Locate every blood parasite and identify its species.
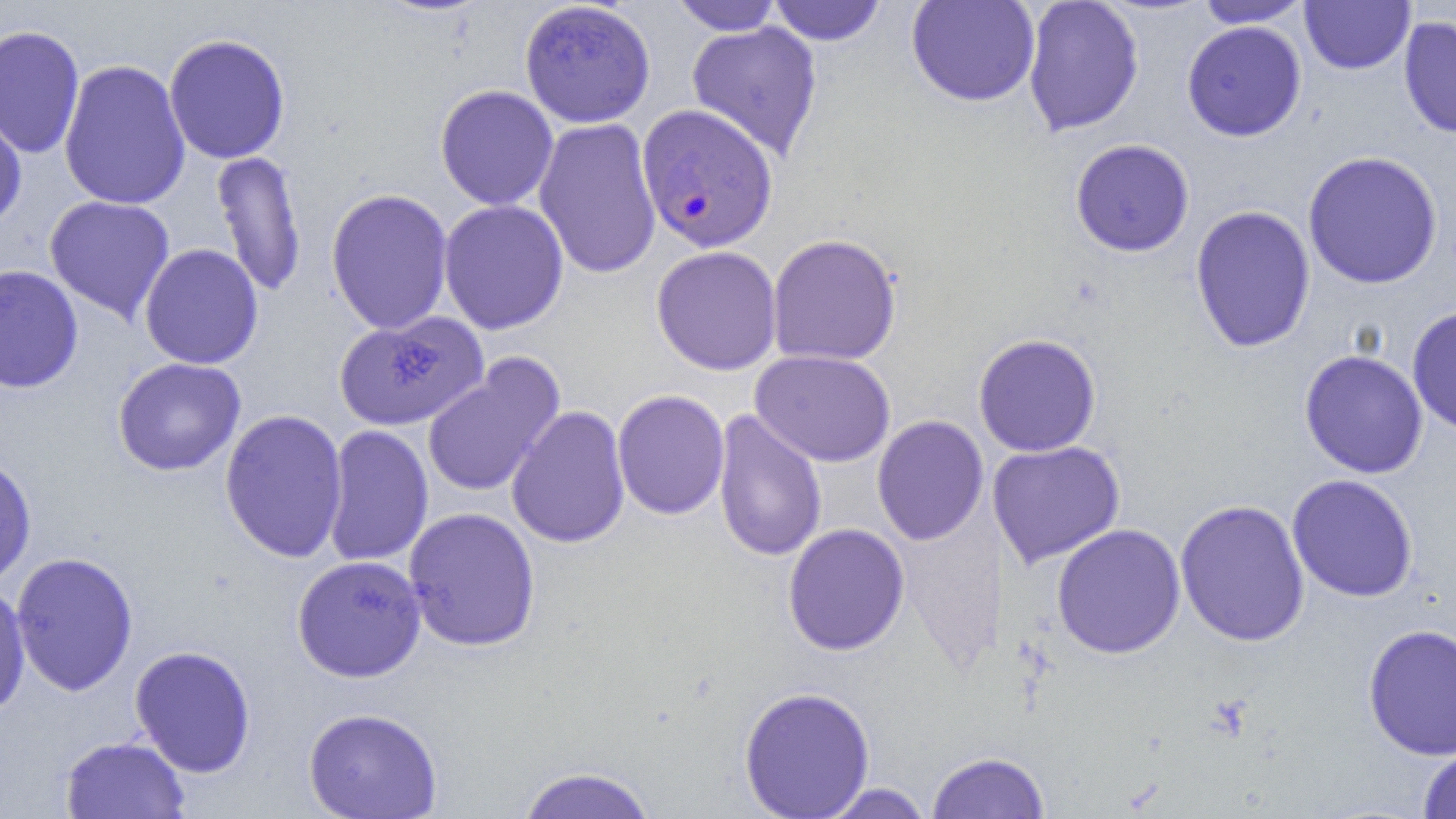

Approximate bounding boxes as (x1, y1, x2, y2) in pixels.
Plasmodium falciparum-infected red blood cells: (636, 104, 778, 253).
No Plasmodium ovale, Plasmodium malariae, Plasmodium vivax, Babesia divergens, or Trypanosoma brucei observed.

Summary:
  - Uninfected red blood cell locations: (669, 0, 786, 35), (906, 0, 1041, 108), (1022, 0, 1145, 137), (1300, 0, 1416, 75), (519, 1, 656, 128), (766, 1, 888, 46), (1195, 1, 1313, 28), (1398, 15, 1456, 139), (1181, 20, 1307, 142), (686, 21, 823, 160), (0, 25, 86, 159), (164, 33, 291, 164), (58, 59, 191, 210), (434, 84, 559, 211), (0, 109, 27, 233), (533, 117, 662, 280), (1069, 139, 1195, 257), (210, 149, 308, 300), (1302, 151, 1443, 289), (326, 187, 454, 335), (44, 195, 176, 325), (438, 199, 569, 335), (1189, 204, 1316, 354), (767, 233, 902, 366), (139, 243, 264, 369), (651, 245, 782, 375), (0, 265, 84, 394), (1407, 306, 1456, 435), (337, 311, 490, 431), (973, 333, 1101, 457), (1299, 349, 1428, 479), (750, 350, 896, 467), (422, 354, 566, 498), (112, 357, 246, 476), (612, 389, 730, 520), (505, 405, 631, 549), (219, 408, 349, 564), (711, 410, 827, 563), (872, 415, 989, 546), (322, 424, 433, 568), (987, 440, 1126, 568), (0, 452, 37, 586), (1287, 474, 1419, 602), (1174, 499, 1310, 647), (403, 507, 541, 651), (896, 512, 1006, 677), (782, 523, 910, 656), (1051, 523, 1186, 659), (10, 552, 139, 696), (291, 554, 427, 683), (0, 580, 31, 720), (1362, 623, 1456, 761), (130, 645, 256, 778), (738, 686, 876, 818), (303, 707, 443, 819), (59, 735, 191, 818), (1418, 746, 1456, 818), (926, 751, 1050, 818), (515, 765, 658, 819), (816, 782, 938, 818)
  - Slide-level diagnosis: Plasmodium falciparum
  - Image size: 1456×819 pixels
  - Modality: light microscopy
  - Preparation: thin blood film
  - Field of view: one of a larger specimen
  - Magnification: 1000x